Identify the parasite.
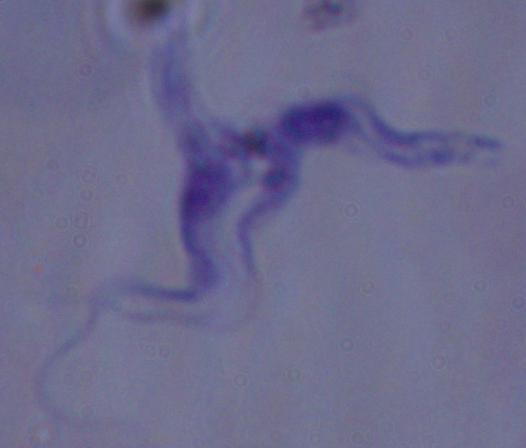

This is a trypanosome.

Captured at 1000x magnification. Photomicrograph.